State which cell type is depicted.
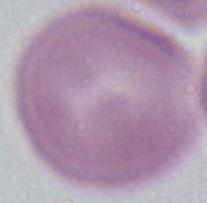

This is an erythrocyte.

Summary:
  - Modality: photomicrograph
  - Magnification: 1000x